Report the malaria status of this cell.
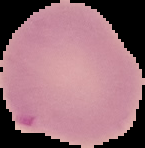
It is uninfected.

Summary:
  - Image size: 145×148 pixels
  - Preparation: thin blood film
  - Image type: cell region segmented out of the field of view; surrounding area masked to black